Identify the parasite.
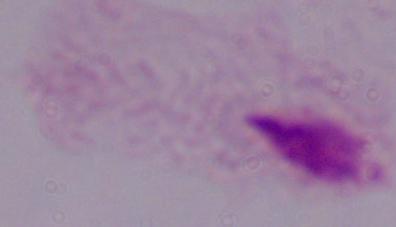
This is a trichomonad.

Summary:
  - Magnification: 1000x
  - Modality: micrograph